Identify the parasite.
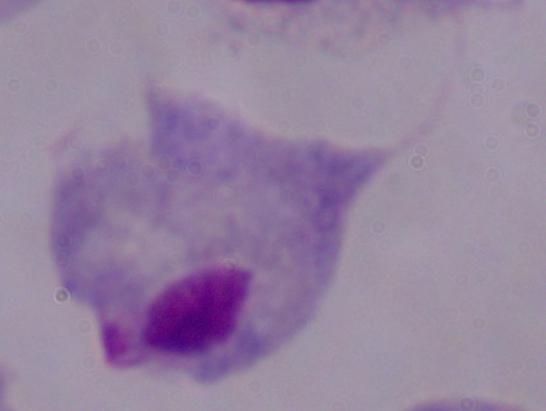

A trichomonad.

Summary:
  - Modality: photomicrograph
  - Magnification: 1000x